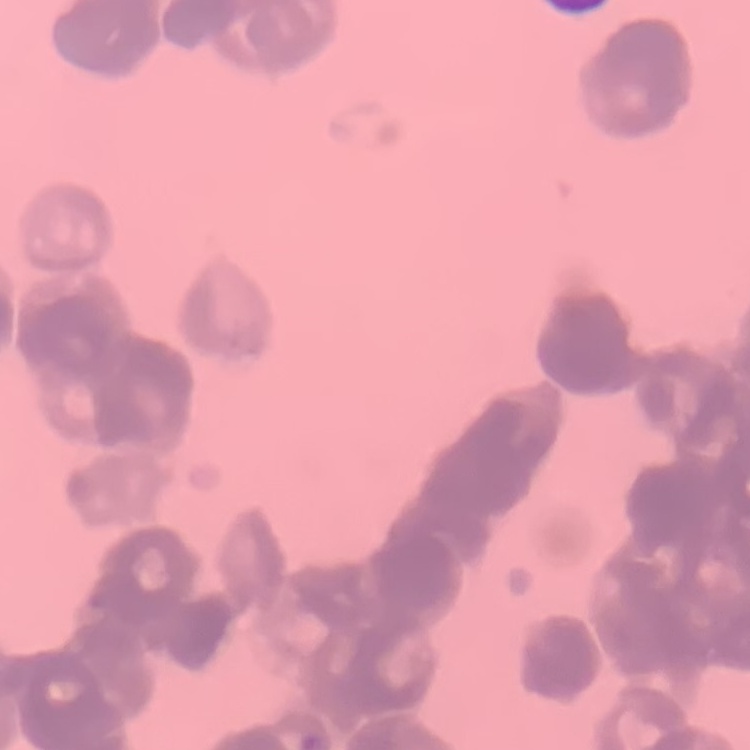

erythrocyte morphology = rouleaux formation
preparation = thin peripheral smear
stain = Field's or Giemsa
image type = square crop of a larger photomicrograph